Look for Plasmodium parasites.
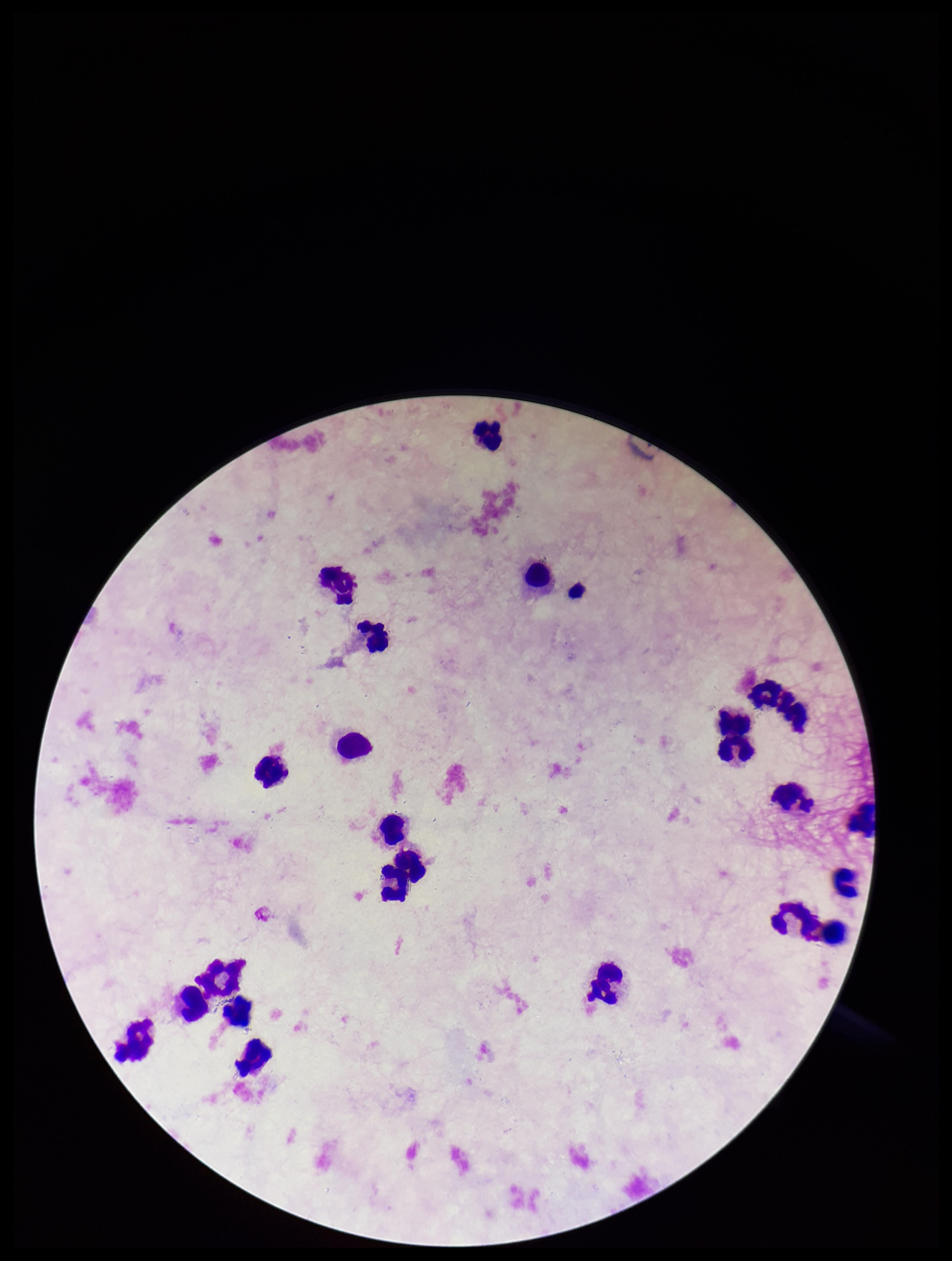
None detected.

One field from this slide. Giemsa stain. Patient malaria status: negative. Leukocyte count: 22. Parasite count: 0. Photographed through the microscope eyepiece with a smartphone camera. Image is 952×1261 pixels. Preparation: thick.